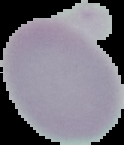
image type = cell region segmented out of the field of view; surrounding area masked to black
result = no malaria parasites seen
image size = 124×145 pixels
preparation = thin blood film